Locate every malaria parasite and every leukocyte.
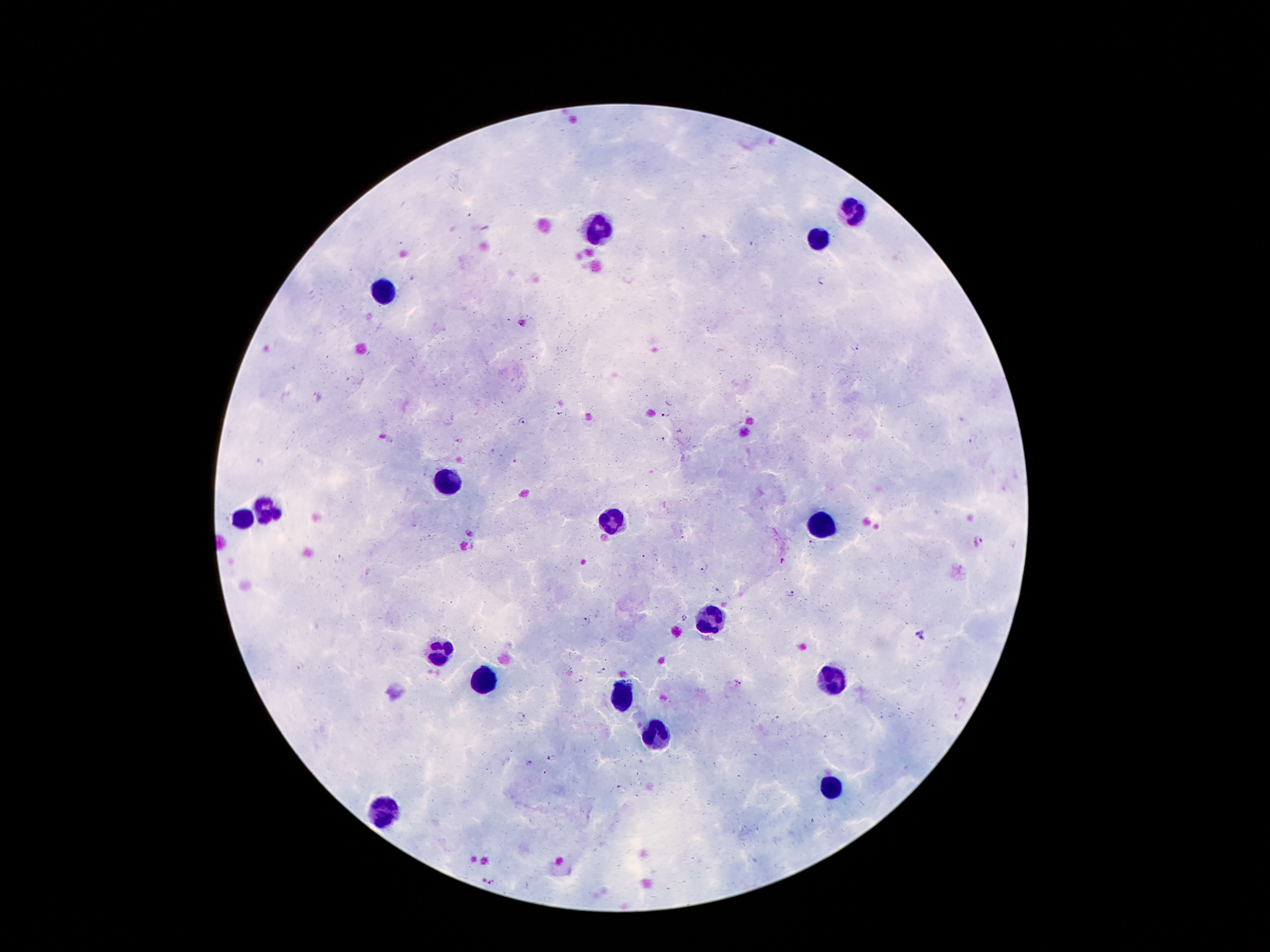
Approximate object centers, in pixels from the top-left corner.
Malaria parasites: (x=823, y=282), (x=522, y=323), (x=856, y=346), (x=663, y=411), (x=522, y=420), (x=663, y=439), (x=973, y=439), (x=460, y=441), (x=978, y=541), (x=813, y=545), (x=782, y=561), (x=704, y=568), (x=791, y=593), (x=684, y=617), (x=586, y=620), (x=303, y=666), (x=601, y=670), (x=737, y=683), (x=521, y=717), (x=776, y=719), (x=551, y=756), (x=529, y=764), (x=621, y=789), (x=488, y=881).
Leukocytes: (x=856, y=210), (x=599, y=227), (x=820, y=236), (x=385, y=290), (x=447, y=483), (x=266, y=510), (x=240, y=520), (x=611, y=524), (x=820, y=526), (x=708, y=619), (x=438, y=650), (x=830, y=677), (x=487, y=683), (x=624, y=698), (x=655, y=734), (x=831, y=790), (x=385, y=811).

Image is 1270×952 pixels. Patient malaria status: infected with Plasmodium falciparum. Thick blood smear. Giemsa-stained preparation. Photographed through the microscope eyepiece with a smartphone camera. Single field of view. 100x magnification.